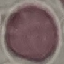
malaria status = uninfected
stain = Giemsa
preparation = thin blood film
image type = cell patch, automatically extracted from a larger field of view and resized to 64 × 64 pixels
capture = smartphone through the microscope eyepiece